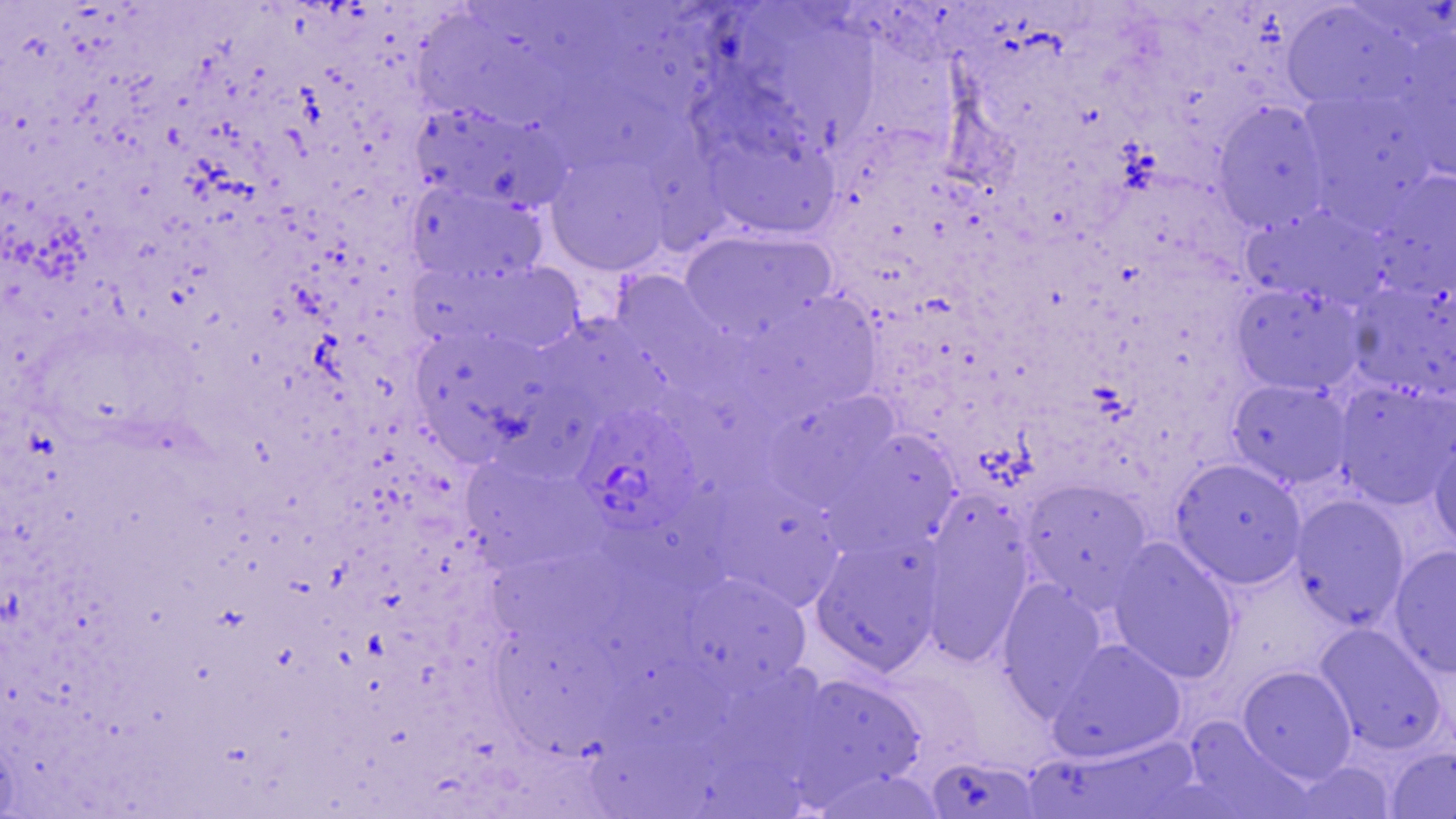

{
  "slide_level_diagnosis": "Plasmodium ovale",
  "image_size": "1456×819 pixels",
  "magnification": "1000x",
  "preparation": "thin blood film",
  "uninfected_red_blood_cell_locations": "approximate bounding boxes as named x1/y1/x2/y2 corners in pixels: (x1=1280, y1=3, x2=1415, y2=112), (x1=416, y1=9, x2=582, y2=125), (x1=786, y1=25, x2=886, y2=152), (x1=1390, y1=44, x2=1455, y2=182), (x1=540, y1=69, x2=688, y2=172), (x1=1299, y1=88, x2=1435, y2=222), (x1=1212, y1=101, x2=1331, y2=232), (x1=425, y1=107, x2=570, y2=213), (x1=642, y1=117, x2=731, y2=253), (x1=705, y1=133, x2=843, y2=242), (x1=544, y1=152, x2=673, y2=276), (x1=1370, y1=170, x2=1456, y2=302), (x1=407, y1=182, x2=543, y2=287), (x1=1241, y1=206, x2=1385, y2=308), (x1=678, y1=230, x2=832, y2=340), (x1=461, y1=260, x2=586, y2=357), (x1=610, y1=274, x2=736, y2=385), (x1=1348, y1=276, x2=1456, y2=404), (x1=1231, y1=283, x2=1365, y2=395), (x1=740, y1=292, x2=882, y2=419), (x1=560, y1=317, x2=674, y2=410), (x1=417, y1=325, x2=546, y2=444), (x1=664, y1=364, x2=782, y2=507), (x1=1227, y1=379, x2=1354, y2=489), (x1=1334, y1=381, x2=1456, y2=508), (x1=761, y1=391, x2=898, y2=506), (x1=834, y1=428, x2=961, y2=550), (x1=1429, y1=433, x2=1456, y2=552), (x1=461, y1=455, x2=602, y2=550), (x1=1171, y1=458, x2=1307, y2=588), (x1=1021, y1=479, x2=1152, y2=605), (x1=728, y1=484, x2=841, y2=612), (x1=603, y1=487, x2=759, y2=577), (x1=1291, y1=496, x2=1409, y2=631), (x1=920, y1=501, x2=1035, y2=662), (x1=810, y1=537, x2=941, y2=676), (x1=1108, y1=538, x2=1238, y2=683), (x1=472, y1=540, x2=630, y2=639), (x1=1389, y1=545, x2=1456, y2=679), (x1=676, y1=574, x2=810, y2=691), (x1=996, y1=581, x2=1107, y2=713), (x1=475, y1=624, x2=615, y2=755), (x1=1315, y1=624, x2=1445, y2=755), (x1=1049, y1=639, x2=1185, y2=762), (x1=606, y1=654, x2=759, y2=746), (x1=1237, y1=666, x2=1356, y2=781), (x1=780, y1=673, x2=927, y2=799), (x1=1190, y1=721, x2=1315, y2=817), (x1=583, y1=723, x2=716, y2=817), (x1=1019, y1=733, x2=1213, y2=818), (x1=1383, y1=746, x2=1455, y2=819), (x1=690, y1=751, x2=815, y2=819), (x1=925, y1=757, x2=1042, y2=817), (x1=1283, y1=760, x2=1399, y2=819)",
  "field_of_view": "single",
  "plasmodium_ovale_infected_red_blood_cell_locations": "approximate bounding boxes as named x1/y1/x2/y2 corners in pixels: (x1=574, y1=406, x2=701, y2=537)",
  "modality": "light microscopy",
  "stain": "May-Grünwald-Giemsa"
}